State the preparation type.
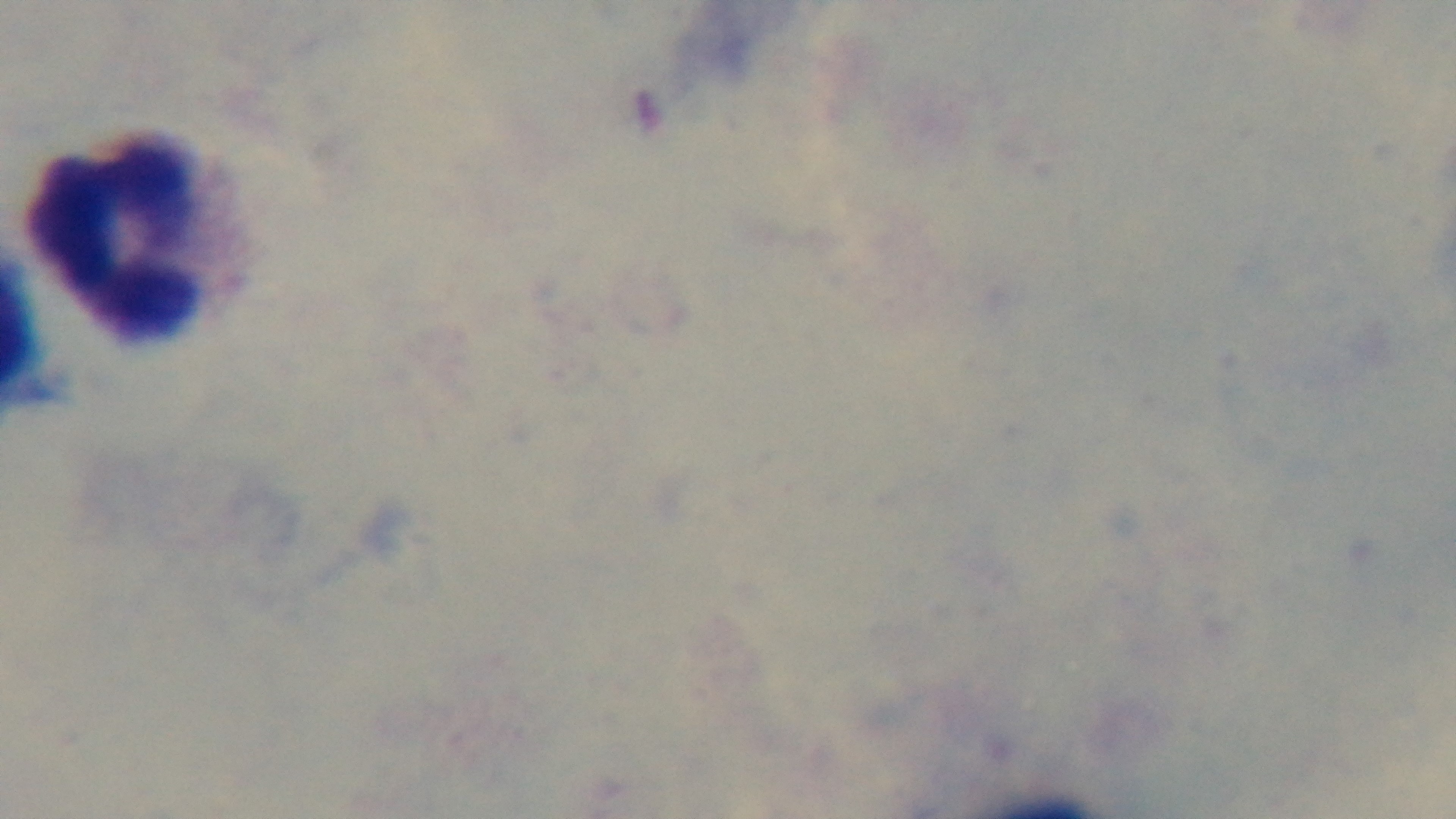

A thick smear.

{
  "objective": "100x oil immersion",
  "field_of_view": "single",
  "capture": "mounted 4K digital camera",
  "stain": "Giemsa",
  "malaria_status": "negative",
  "modality": "light microscopy"
}